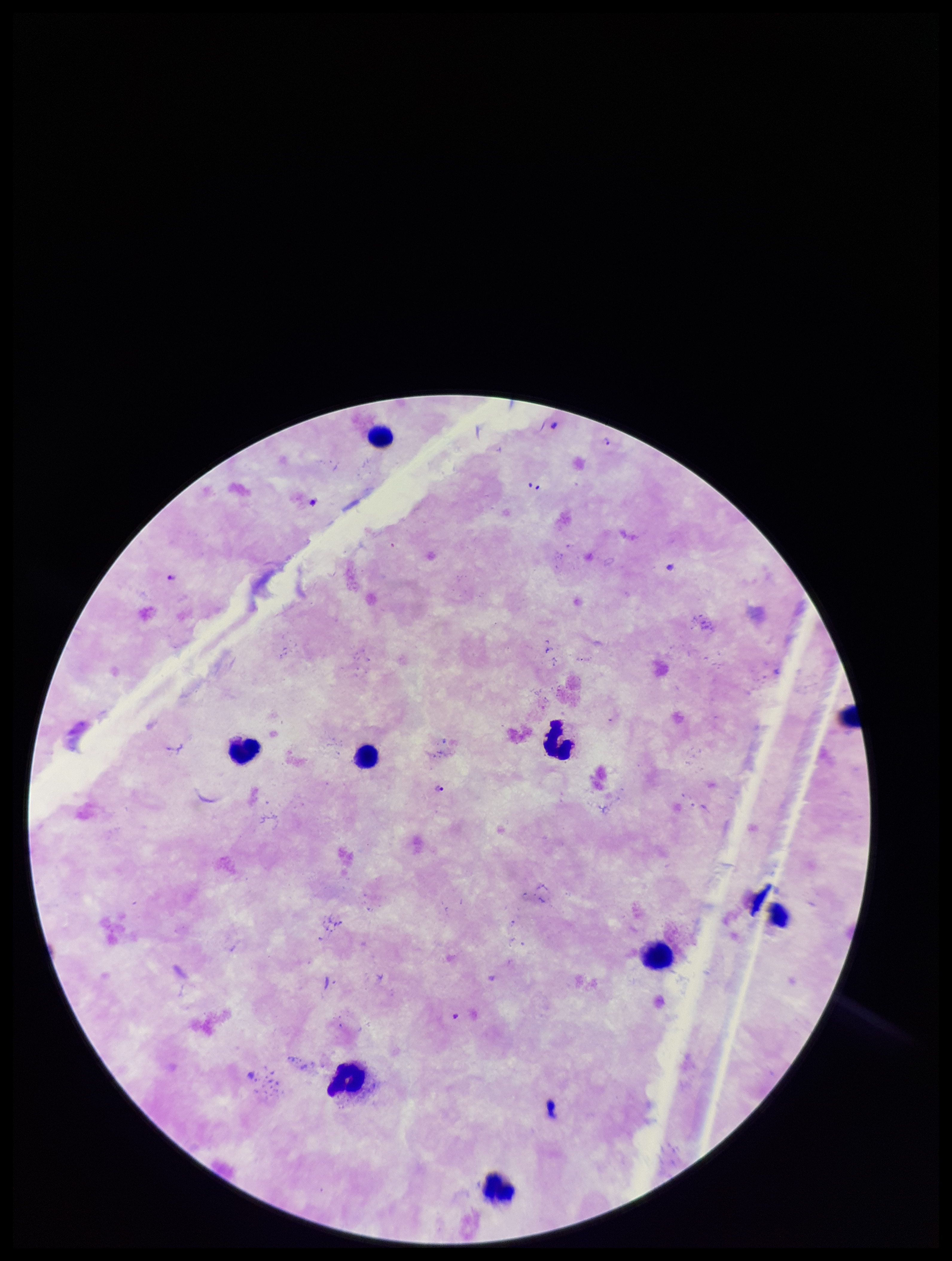 Stained with Giemsa. Single field of view. Leukocyte count: 9. Patient malaria status: infected. Plasmodium parasites: detected. Image is 952×1261 pixels. Photographed through the microscope eyepiece with a smartphone camera. Species reported for this patient: Plasmodium falciparum. Preparation: thick smear. Parasite count: 3.